Look for Plasmodium parasites.
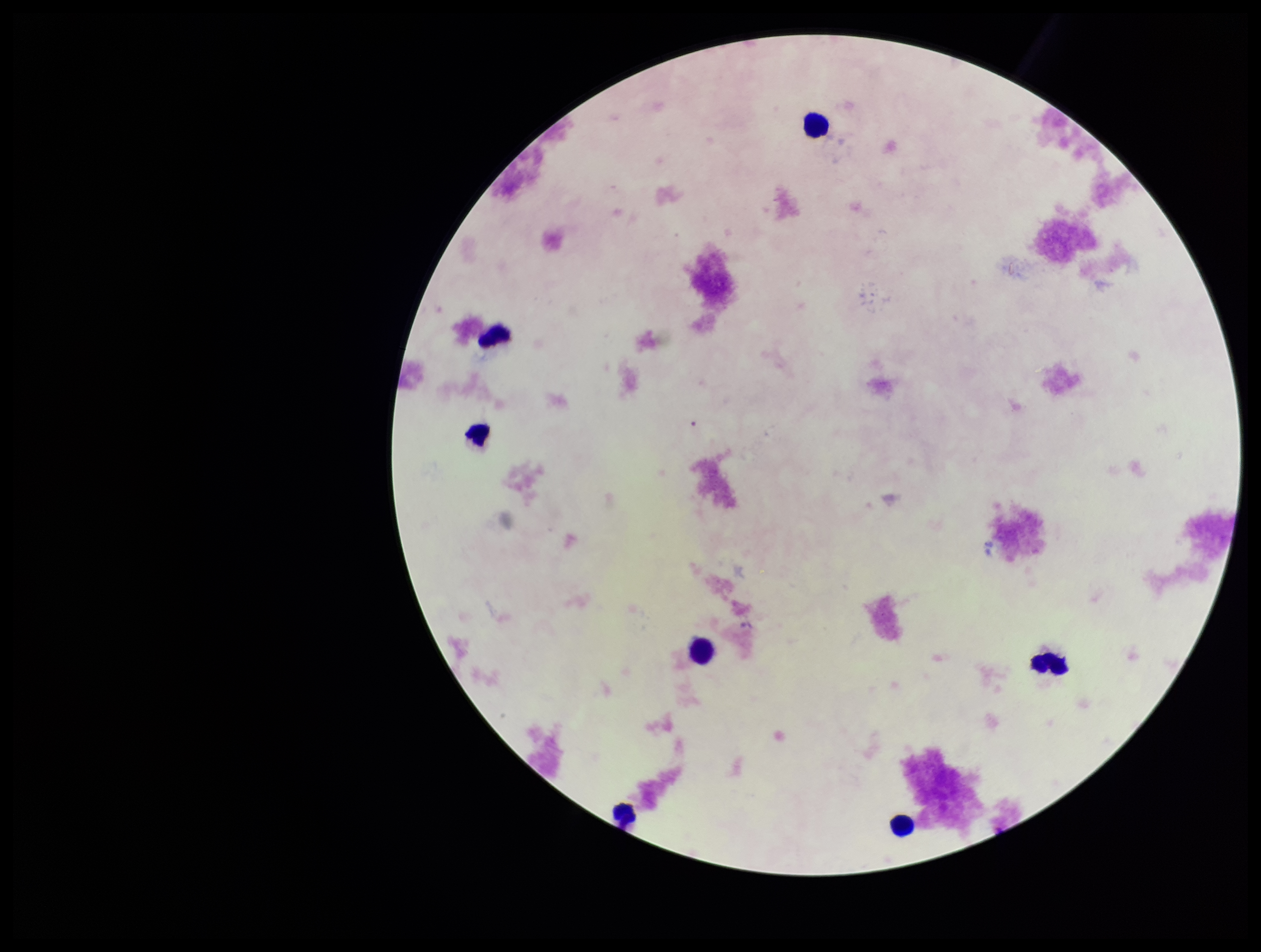

None detected.

Summary:
  - Preparation: thick smear
  - Stain: Giemsa
  - Capture: smartphone photograph through the microscope eyepiece
  - Image size: 1261×952 pixels
  - Leukocyte count: 7
  - Parasite count: 0
  - Patient malaria status: negative
  - Field of view: single